Give the position of every leukocyte visible.
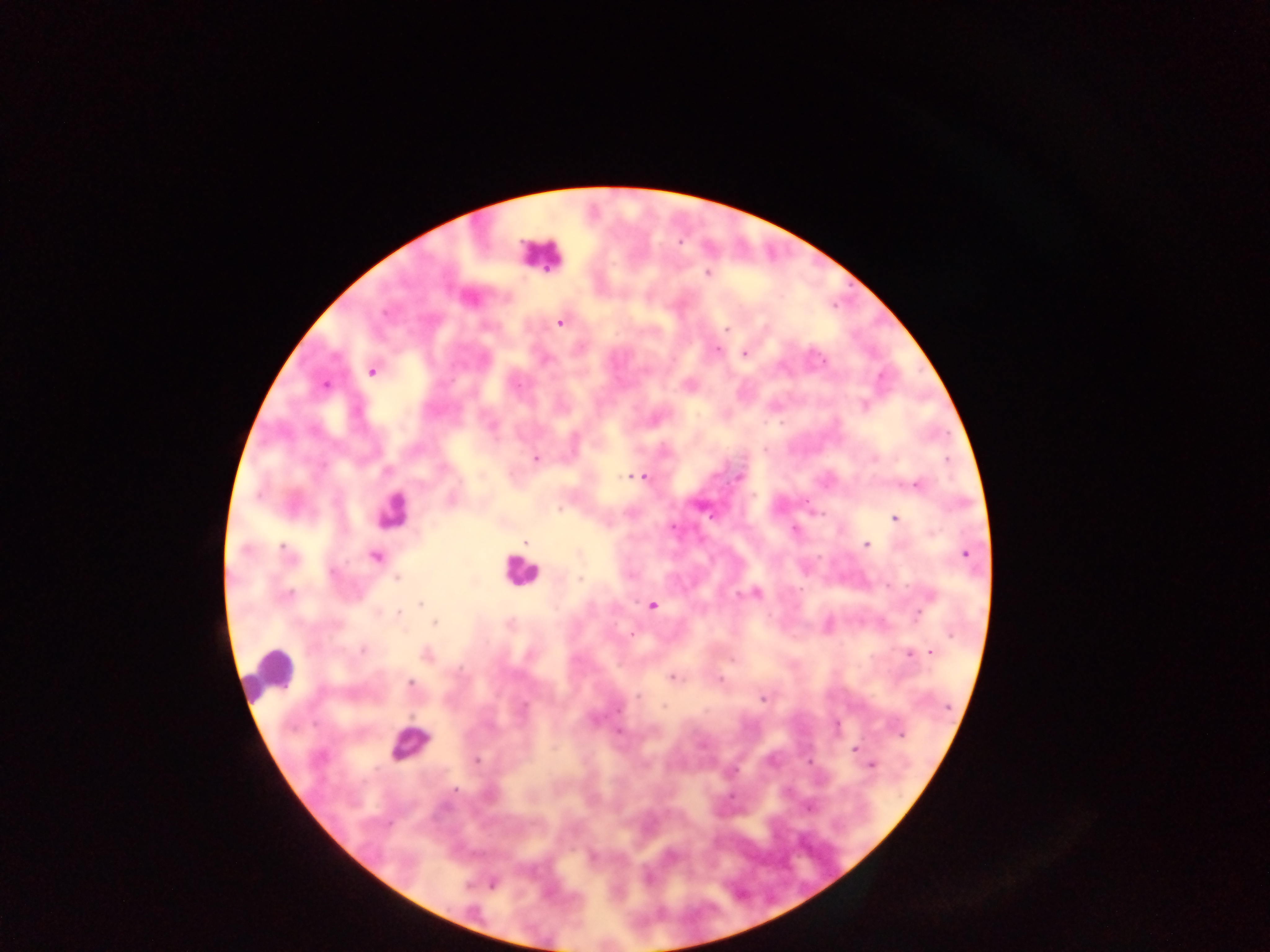
Approximate centers as (x, y) in pixels.
Leukocytes: (539, 255), (390, 511), (518, 571), (270, 672), (410, 744).

plasmodium_parasite_locations: 'approximate centers as (x, y) in pixels: (708, 274), (560, 321), (727, 329), (716, 349), (745, 353), (372, 370), (325, 384), (864, 405), (535, 458), (642, 476), (738, 476), (632, 477), (916, 484), (894, 518), (525, 541), (866, 545), (964, 553), (375, 556), (396, 578), (755, 592), (421, 603), (652, 606), (398, 614), (434, 623), (907, 652), (931, 652), (427, 654), (733, 661), (671, 677), (718, 680), (410, 684), (762, 698), (618, 731), (900, 733), (855, 749), (476, 760), (872, 765), (733, 796), (492, 883)'
field_of_view: single
capture: mobile-phone photograph through a microscope
image_size: 1270×952 pixels
country: Ghana
preparation: thick blood smear